Give the extent of all Babesia divergens-infected red blood cells.
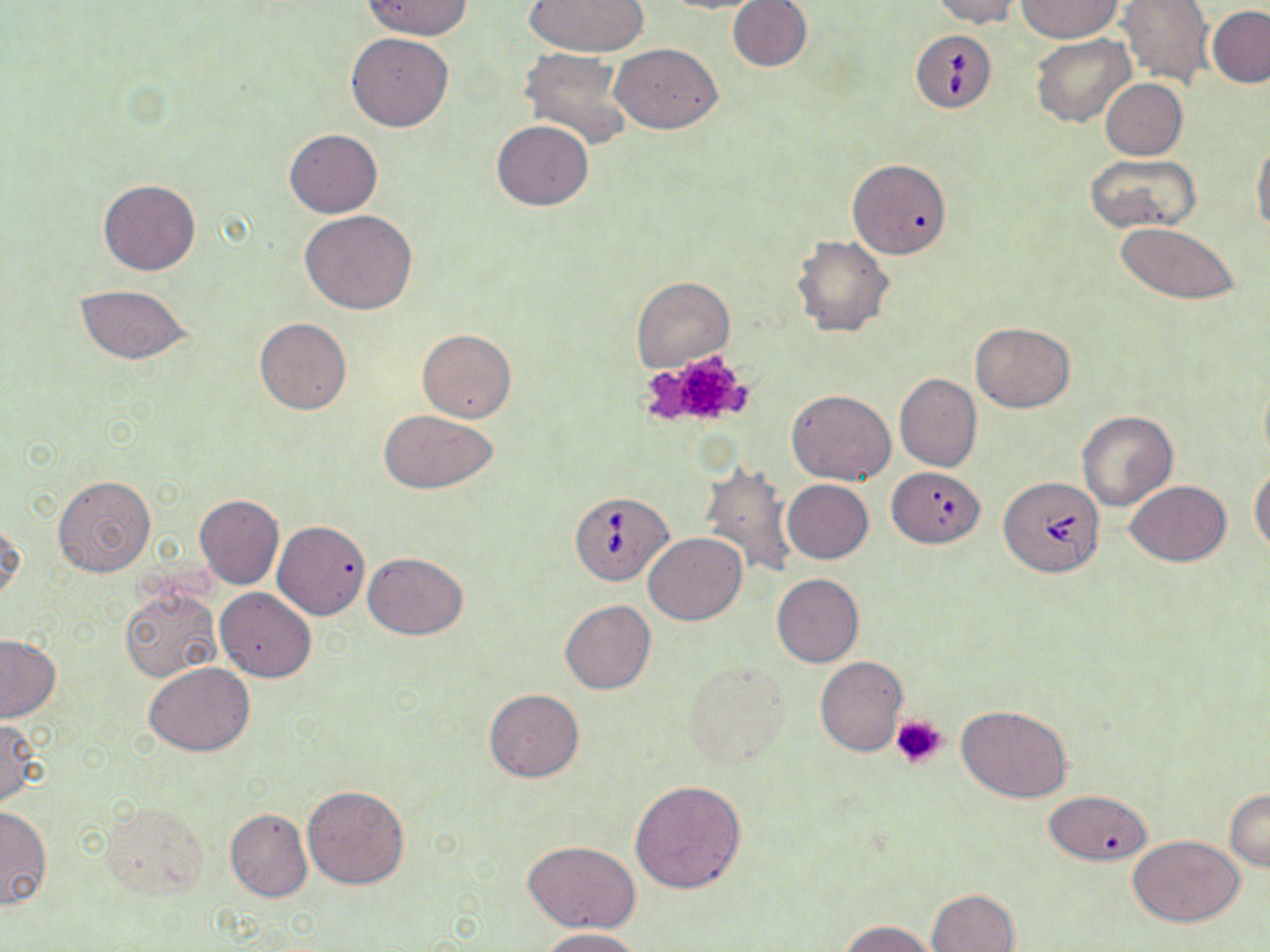

Approximate bounding boxes as (x1,y1)-(x2,y2) corner pairs in pixels.
Babesia divergens-infected red blood cells: (912,29)-(998,113), (998,476)-(1105,576), (569,490)-(673,588).

slide-level diagnosis = Babesia divergens
magnification = 1000x
preparation = thin blood film
stain = May-Grünwald-Giemsa
image size = 1270×952 pixels
platelet locations = approximate bounding boxes as (x1,y1)-(x2,y2) corner pairs in pixels: (645,348)-(757,430), (891,714)-(949,769)
modality = light microscopy
uninfected red blood cell locations = approximate bounding boxes as (x1,y1)-(x2,y2) corner pairs in pixels: (363,0)-(473,39), (523,0)-(649,57), (657,0)-(768,14), (728,0)-(811,71), (930,0)-(1021,26), (1117,0)-(1214,88), (1014,1)-(1121,41), (1207,6)-(1270,88), (347,32)-(453,131), (1030,33)-(1134,127), (610,43)-(722,134), (520,49)-(636,151), (1100,78)-(1188,160), (491,120)-(594,211), (285,129)-(382,218), (1252,139)-(1270,235), (1085,153)-(1202,233), (847,158)-(951,258), (98,178)-(201,276), (300,210)-(417,314), (1115,222)-(1244,306), (791,235)-(895,337), (632,276)-(735,371), (74,284)-(192,364), (255,317)-(352,415), (972,323)-(1075,412), (417,328)-(515,423), (894,373)-(984,472), (1260,377)-(1270,465), (787,390)-(896,485), (378,410)-(498,493), (1077,410)-(1177,510), (700,461)-(798,579), (1250,462)-(1270,554), (888,467)-(986,548), (53,476)-(155,577), (783,479)-(873,563), (1125,480)-(1232,565), (194,495)-(283,589), (0,518)-(24,606), (273,520)-(370,619), (644,531)-(746,625), (362,553)-(470,639), (772,574)-(864,668), (120,587)-(220,682), (215,588)-(316,681), (560,599)-(655,693), (0,634)-(60,723), (816,656)-(908,755), (683,660)-(789,770), (144,662)-(256,755), (484,689)-(584,781), (957,706)-(1072,802), (0,719)-(43,808), (630,779)-(748,894), (302,785)-(410,888), (1225,788)-(1270,870), (1043,789)-(1153,865), (100,802)-(209,901), (0,806)-(52,909), (225,809)-(312,901), (1130,836)-(1243,927), (523,840)-(640,931), (929,889)-(1020,952), (842,920)-(937,952), (539,927)-(645,952)
field of view = single